Classify this cell by malaria status.
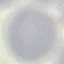

Uninfected.

Summary:
  - Stain: Giemsa
  - Preparation: thin smear
  - Capture: smartphone camera at the microscope eyepiece
  - Image type: cell patch, automatically extracted from a larger field of view and resized to 64 × 64 pixels